Assess the morphology of the erythrocytes.
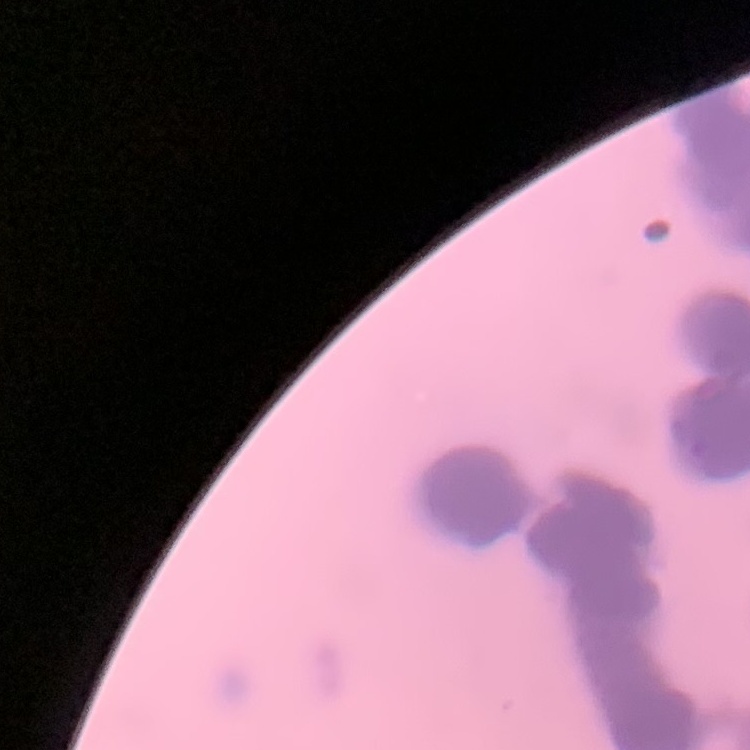
They show rouleaux formation.

Field's or Giemsa stain. Thin peripheral smear. One tile cut from a larger photomicrograph.